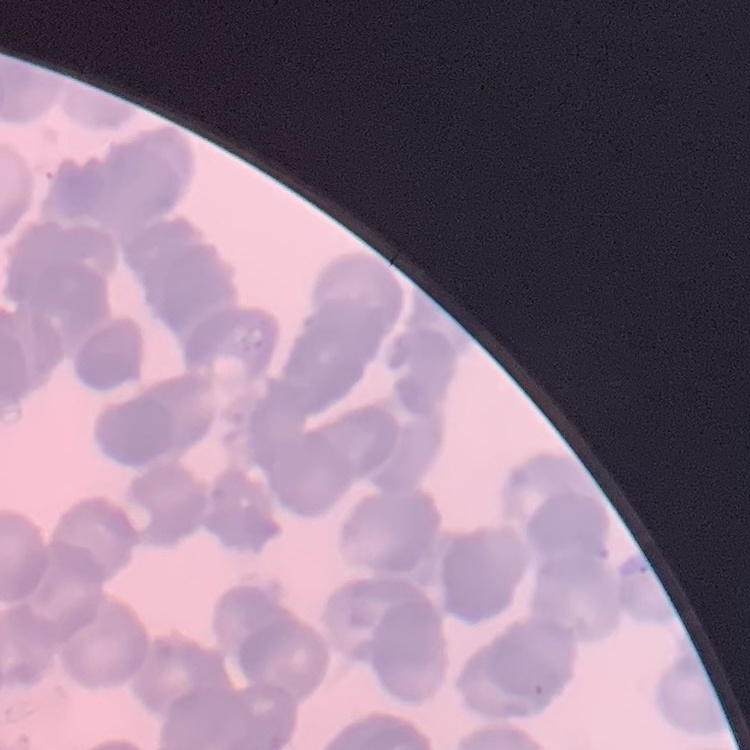
The red blood cells show rouleaux formation. One tile cut from a larger photomicrograph. Field's or Giemsa stain. Thin peripheral smear.